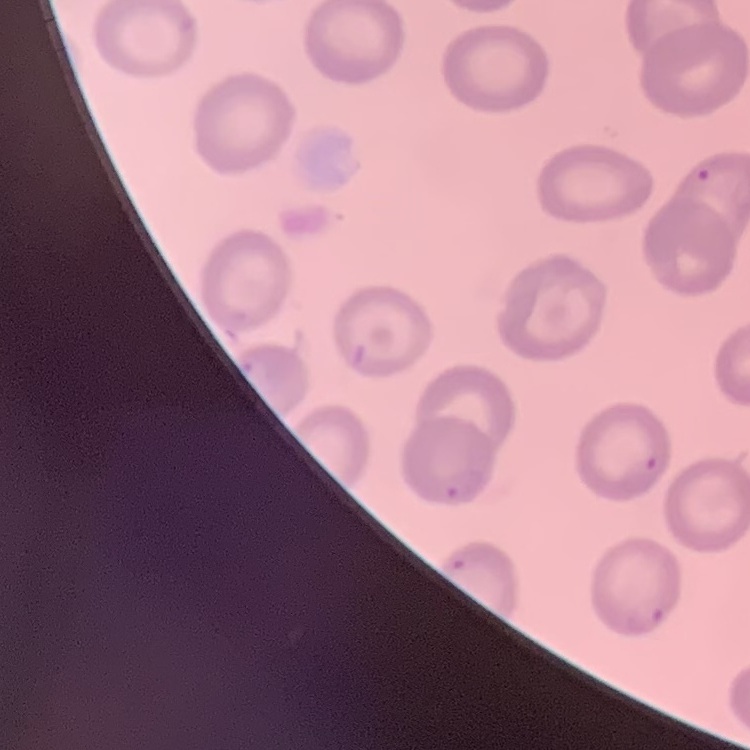
The red blood cells exhibit no rouleaux formation. Thin peripheral smear. One tile cut from a larger photomicrograph. Stained with either Field's or Giemsa.